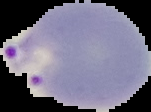

Cell region segmented out of the field of view; the surrounding area is masked to black. Image is 151×112 pixels. Result: malaria parasites detected. From a thin blood film.